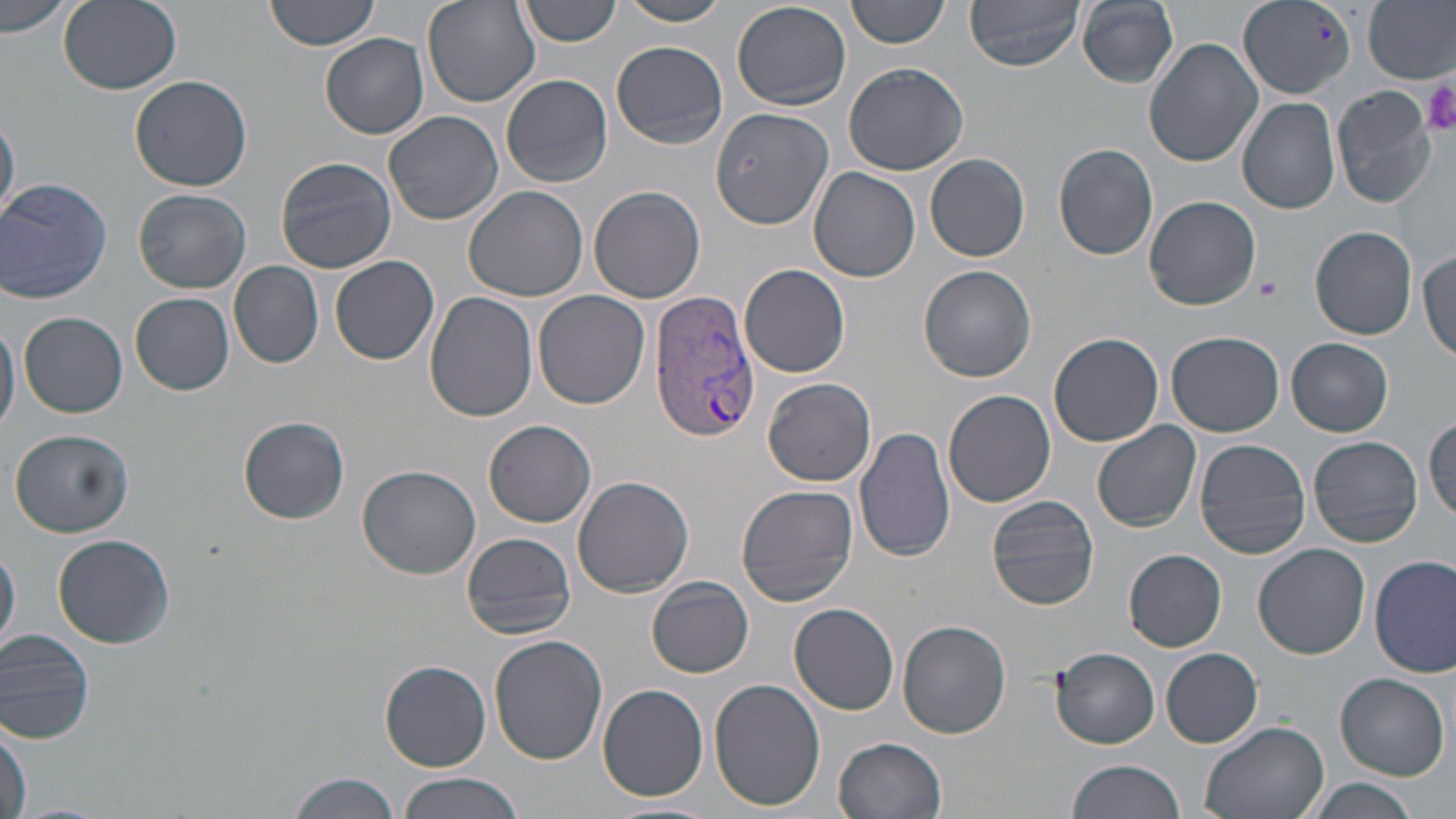
Approximate bounding boxes as [x1, y1, x2, y2] in pixels. Uninfected red blood cell locations: [0, 0, 76, 40], [59, 0, 181, 94], [266, 0, 381, 51], [421, 0, 539, 107], [519, 0, 622, 46], [619, 0, 730, 26], [845, 0, 950, 49], [964, 0, 1086, 71], [1364, 0, 1456, 84], [1073, 1, 1181, 88], [1240, 1, 1357, 99], [732, 3, 852, 110], [320, 32, 429, 138], [1144, 38, 1264, 169], [610, 39, 727, 149], [842, 62, 969, 176], [130, 73, 253, 191], [501, 73, 614, 187], [1331, 85, 1439, 207], [1238, 97, 1340, 215], [383, 110, 503, 224], [712, 114, 841, 239], [0, 117, 20, 221], [1172, 119, 1288, 258], [1053, 143, 1157, 260], [926, 153, 1030, 262], [274, 156, 398, 274], [807, 166, 921, 282], [2, 178, 111, 306], [463, 184, 588, 302], [588, 186, 705, 303], [134, 189, 252, 293], [1144, 195, 1261, 311], [1311, 227, 1417, 340], [1415, 250, 1456, 366], [331, 254, 440, 365], [230, 261, 324, 369], [742, 264, 850, 378], [918, 264, 1037, 383], [535, 290, 650, 409], [131, 293, 235, 396], [424, 294, 537, 424], [19, 312, 128, 417], [0, 314, 20, 439], [1168, 330, 1284, 436], [1048, 331, 1164, 446], [1287, 338, 1393, 435], [763, 377, 876, 488], [944, 390, 1057, 508], [1427, 414, 1456, 526], [238, 416, 350, 524], [485, 419, 596, 527], [1092, 420, 1203, 532], [855, 426, 955, 564], [8, 428, 136, 537], [1309, 435, 1423, 548], [1193, 439, 1311, 559], [358, 464, 480, 579], [571, 475, 694, 597], [737, 483, 859, 606], [986, 495, 1100, 611], [460, 530, 577, 640], [52, 535, 174, 649], [1254, 544, 1370, 661], [0, 545, 20, 654], [1124, 549, 1226, 650], [1369, 555, 1456, 678], [647, 577, 755, 678], [788, 603, 900, 715], [897, 617, 1011, 739], [0, 626, 100, 743], [489, 635, 607, 765], [1051, 648, 1161, 749], [1161, 648, 1264, 748], [381, 658, 491, 771], [1334, 672, 1449, 779], [709, 676, 826, 811], [597, 683, 709, 802], [1199, 718, 1331, 818], [1, 721, 30, 815], [834, 735, 947, 819], [1065, 759, 1187, 819], [288, 772, 402, 819], [397, 773, 527, 819], [1306, 778, 1421, 819], [2, 801, 118, 819], [601, 801, 719, 819]. Plasmodium vivax-infected red blood cell locations: [649, 291, 759, 442]. Platelet locations: [1422, 81, 1456, 139], [1257, 275, 1282, 301]. Slide-level diagnosis: Plasmodium vivax. Light microscopy. Thin blood smear. Image is 1456×819 pixels. One field of a larger specimen. Captured at 1000x magnification. May-Grünwald-Giemsa-stained preparation.